Give the preparation type.
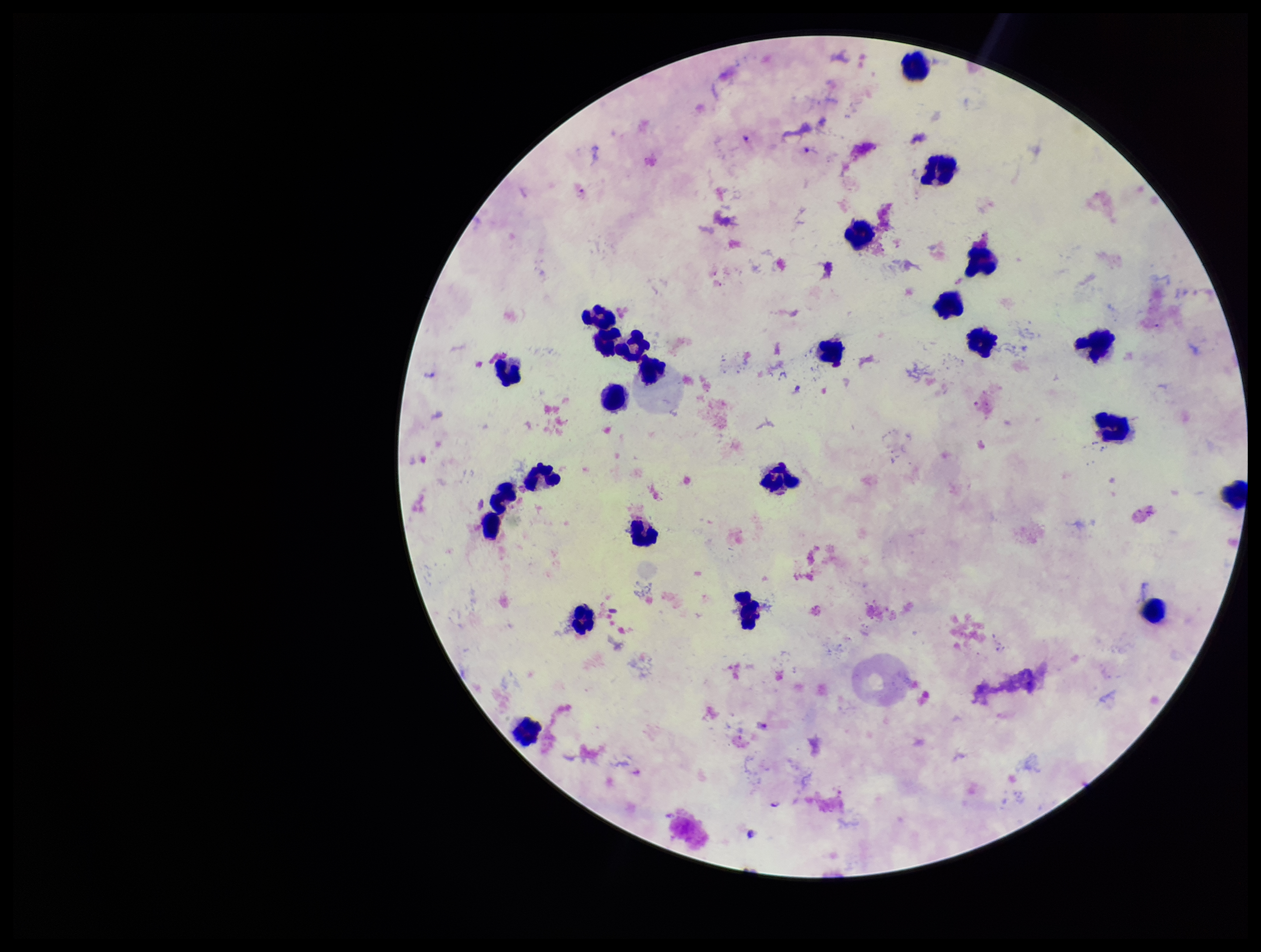
It is a thick blood smear.

{
  "patient_malaria_status": "infected",
  "leukocyte_count": 25,
  "parasite_count": 3,
  "capture": "smartphone photograph through the microscope eyepiece",
  "field_of_view": "one from this slide",
  "image_size": "1261×952 pixels",
  "species_reported_for_this_patient": "Plasmodium falciparum",
  "stain": "Giemsa",
  "plasmodium_parasites": "identified"
}